State which parasite is depicted.
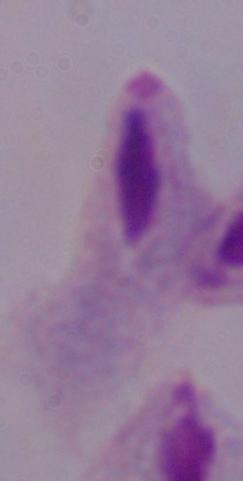

A trichomonad.

magnification: 1000x
modality: photomicrograph